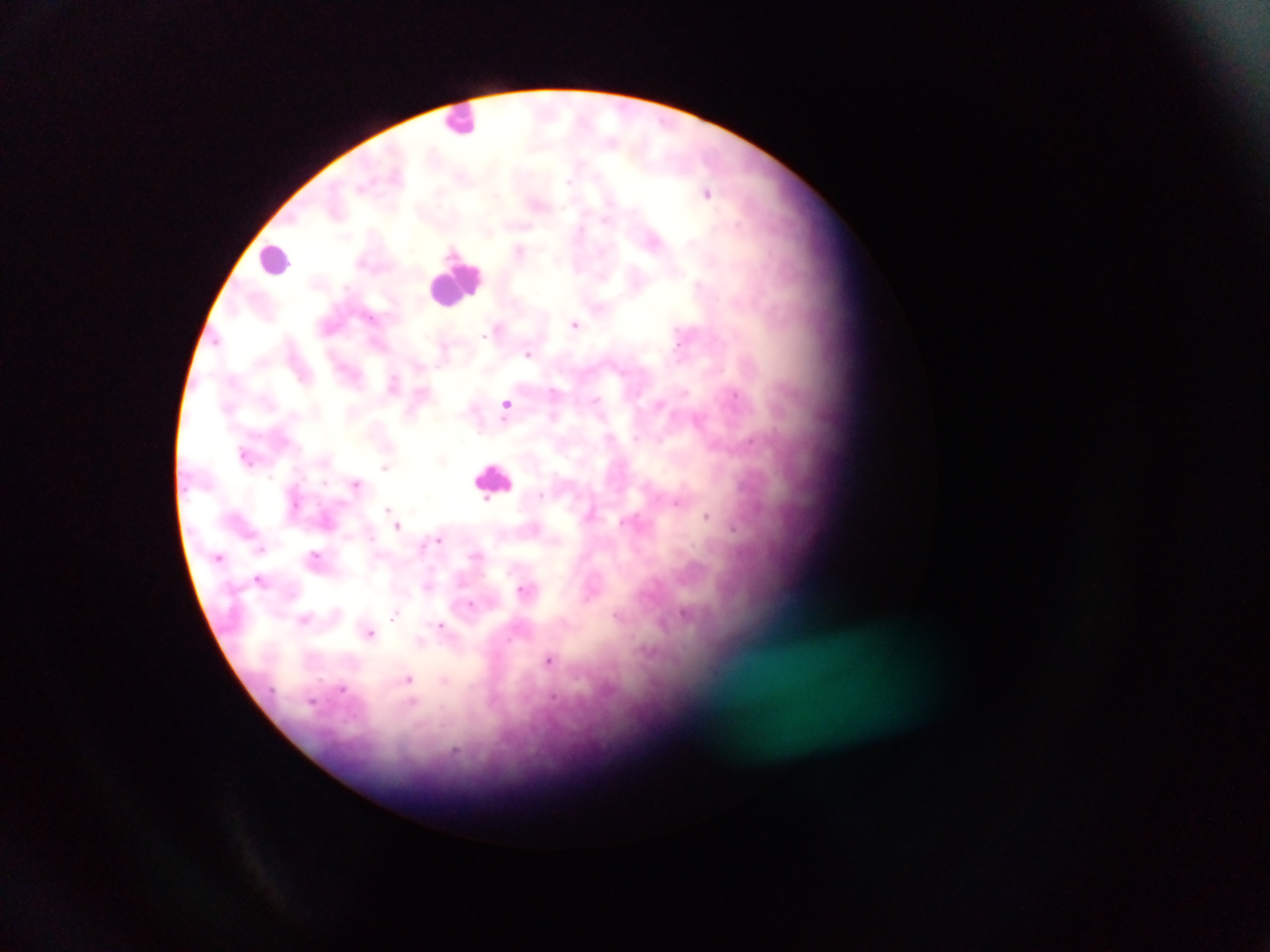
image_size: 1270×952 pixels
leukocyte_locations: 'approximate centers as x y in pixels: 461 120; 275 258; 456 281; 494 479'
preparation: thick blood film
field_of_view: single
capture: mobile-phone photograph through a microscope
plasmodium_parasite_locations: 'approximate centers as x y in pixels: 708 192; 538 202; 655 240; 520 250; 576 323; 499 328; 529 352; 394 383; 506 404; 699 418; 246 455; 386 466; 356 483; 387 511; 591 512; 706 515; 398 524; 734 527; 440 539; 262 547; 219 556; 315 556; 260 579; 525 589; 471 604; 396 615; 619 615; 305 619; 664 622; 442 626; 369 632; 421 641; 551 659; 409 679'
country: Ghana